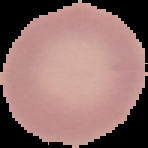
{
  "image_size": "148×148 pixels",
  "result": "negative for malaria parasites",
  "image_type": "cell region segmented out of the field of view; surrounding area masked to black",
  "preparation": "thin blood film"
}